Outline each blood parasite and name the species.
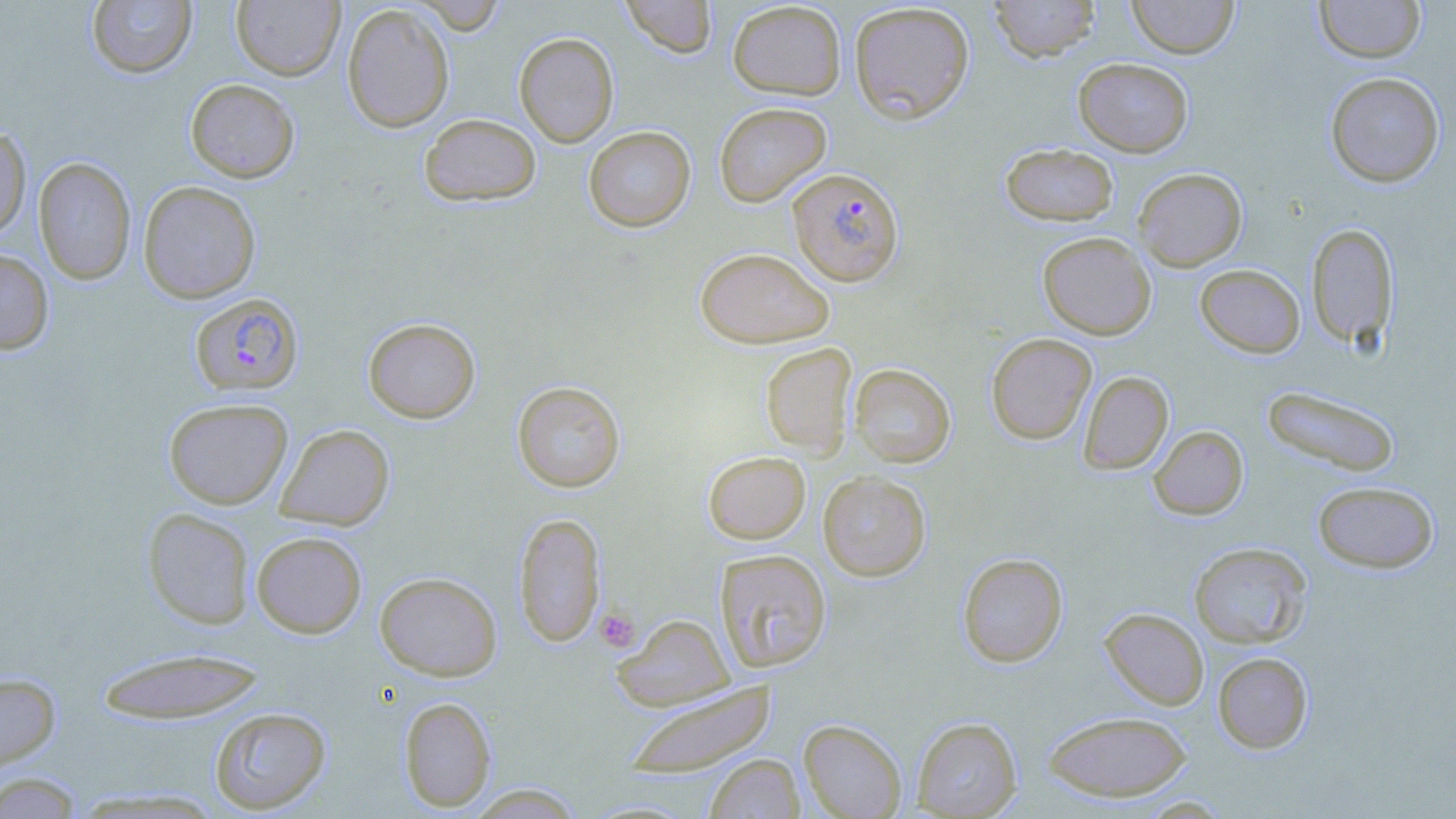

Approximate bounding boxes as named x1/y1/x2/y2 corners in pixels.
Plasmodium falciparum-infected red blood cells: (x1=787, y1=167, x2=904, y2=286), (x1=190, y1=293, x2=304, y2=396).
No Plasmodium ovale, Plasmodium malariae, Plasmodium vivax, Babesia divergens, or Trypanosoma brucei observed.

slide-level diagnosis = Plasmodium falciparum
image size = 1456×819 pixels
magnification = 1000x
platelet locations = approximate bounding boxes as named x1/y1/x2/y2 corners in pixels: (x1=595, y1=607, x2=641, y2=652)
stain = May-Grünwald-Giemsa
uninfected red blood cell locations = approximate bounding boxes as named x1/y1/x2/y2 corners in pixels: (x1=231, y1=0, x2=345, y2=81), (x1=411, y1=0, x2=507, y2=35), (x1=620, y1=0, x2=718, y2=58), (x1=988, y1=0, x2=1101, y2=62), (x1=1127, y1=0, x2=1239, y2=59), (x1=1314, y1=0, x2=1425, y2=63), (x1=87, y1=1, x2=197, y2=78), (x1=727, y1=1, x2=846, y2=100), (x1=849, y1=2, x2=975, y2=124), (x1=342, y1=3, x2=455, y2=133), (x1=514, y1=32, x2=619, y2=147), (x1=1073, y1=58, x2=1193, y2=157), (x1=1325, y1=71, x2=1445, y2=188), (x1=186, y1=79, x2=300, y2=182), (x1=714, y1=102, x2=832, y2=207), (x1=419, y1=113, x2=541, y2=206), (x1=0, y1=125, x2=31, y2=240), (x1=583, y1=125, x2=696, y2=232), (x1=1000, y1=142, x2=1119, y2=226), (x1=34, y1=157, x2=136, y2=285), (x1=1133, y1=167, x2=1247, y2=271), (x1=137, y1=181, x2=261, y2=304), (x1=1306, y1=222, x2=1398, y2=350), (x1=1037, y1=232, x2=1156, y2=340), (x1=694, y1=247, x2=834, y2=348), (x1=0, y1=249, x2=54, y2=354), (x1=1195, y1=264, x2=1305, y2=358), (x1=363, y1=317, x2=481, y2=423), (x1=986, y1=332, x2=1096, y2=445), (x1=760, y1=342, x2=857, y2=458), (x1=849, y1=363, x2=956, y2=468), (x1=1078, y1=371, x2=1174, y2=475), (x1=512, y1=380, x2=626, y2=493), (x1=1261, y1=385, x2=1401, y2=477), (x1=163, y1=398, x2=293, y2=509), (x1=275, y1=423, x2=395, y2=530), (x1=1149, y1=426, x2=1248, y2=520), (x1=703, y1=451, x2=811, y2=544), (x1=818, y1=471, x2=931, y2=581), (x1=1312, y1=480, x2=1439, y2=574), (x1=142, y1=508, x2=255, y2=629), (x1=514, y1=512, x2=605, y2=647), (x1=251, y1=531, x2=367, y2=637), (x1=1188, y1=542, x2=1313, y2=649), (x1=714, y1=549, x2=832, y2=673), (x1=957, y1=552, x2=1068, y2=667), (x1=375, y1=571, x2=502, y2=680), (x1=1100, y1=607, x2=1209, y2=709), (x1=611, y1=613, x2=735, y2=711), (x1=95, y1=647, x2=268, y2=723), (x1=1212, y1=652, x2=1313, y2=754), (x1=0, y1=671, x2=60, y2=771), (x1=623, y1=681, x2=778, y2=778), (x1=399, y1=696, x2=496, y2=812), (x1=208, y1=706, x2=331, y2=814), (x1=1043, y1=710, x2=1192, y2=802), (x1=912, y1=716, x2=1022, y2=818), (x1=798, y1=719, x2=907, y2=819), (x1=704, y1=754, x2=804, y2=818), (x1=0, y1=772, x2=84, y2=818), (x1=465, y1=784, x2=586, y2=818)
preparation = thin blood smear
modality = optical microscopy
field of view = single